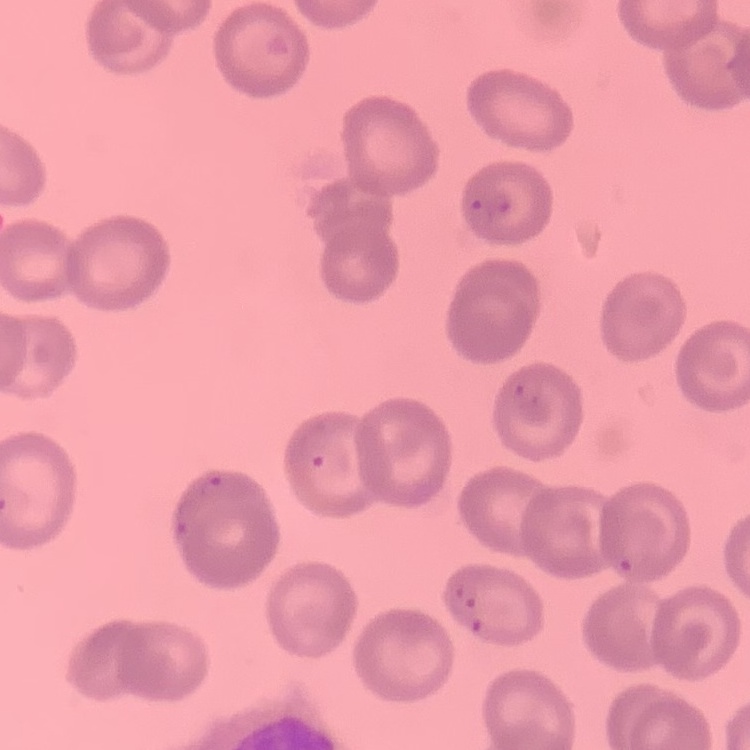
Summary:
  - Erythrocyte morphology: no rouleaux formation
  - Stain: Field's or Giemsa
  - Preparation: thin blood film
  - Image type: square crop of a larger photomicrograph